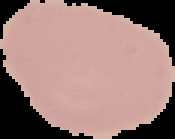

The area outside the segmented cell region is set to black. Result: no malaria parasites detected. From a thin blood film. Image is 175×139 pixels.